Report the malaria status of this cell.
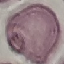
Uninfected.

{
  "preparation": "thin blood smear",
  "image_type": "automatically extracted cell patch, resized to 64 × 64 pixels",
  "capture": "smartphone through the microscope eyepiece",
  "stain": "Giemsa"
}